Point out each Plasmodium parasite and each leukocyte.
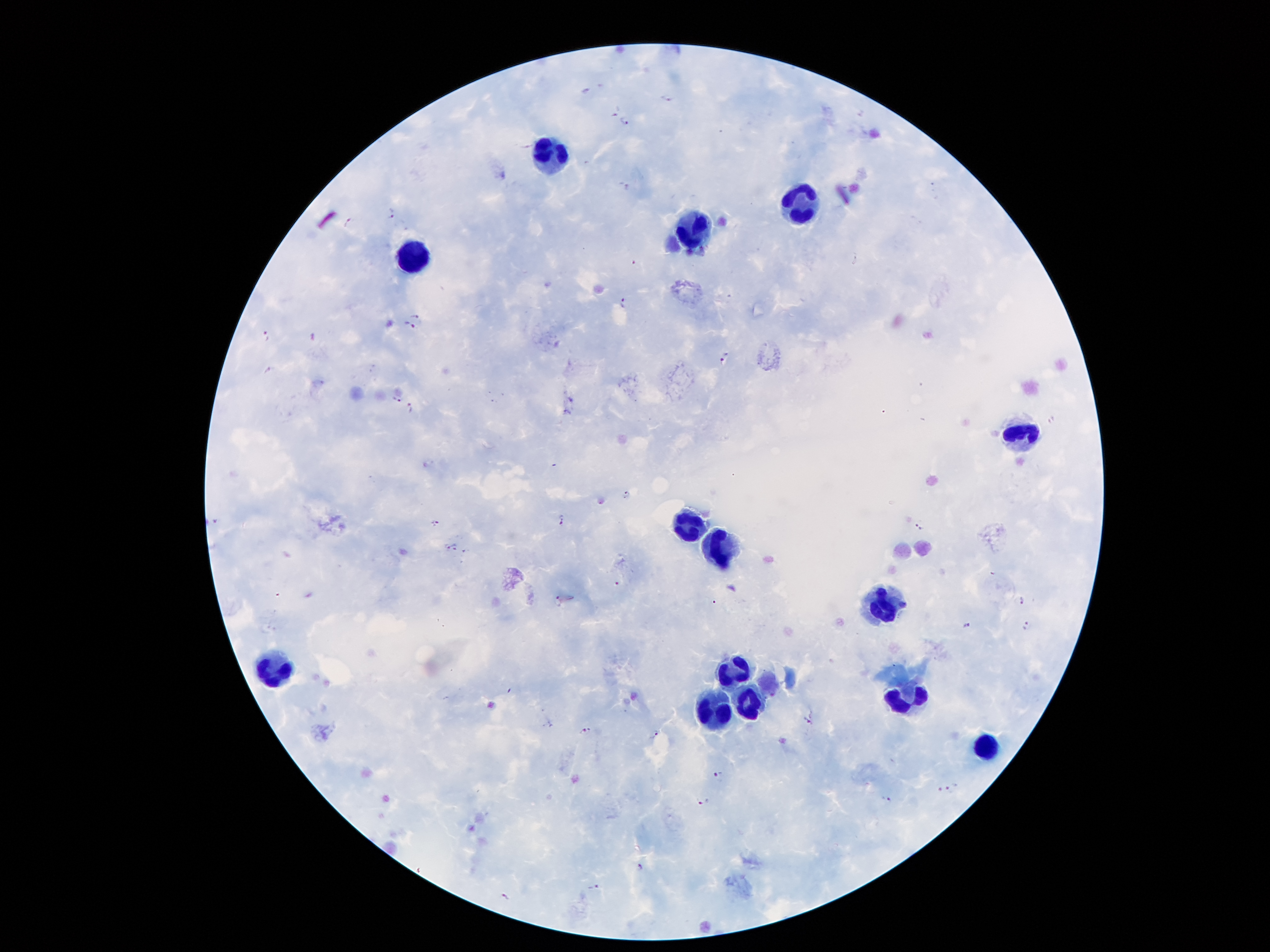

Approximate centers as [x, y] in pixels.
Plasmodium parasites: [587, 91], [669, 98], [624, 121], [627, 186], [391, 212], [347, 221], [622, 301], [419, 315], [409, 325], [266, 335], [724, 359], [270, 370], [394, 399], [410, 407], [627, 496], [560, 519], [434, 523], [918, 526], [446, 546], [455, 548], [618, 584], [559, 599], [1023, 601], [967, 625], [1026, 625], [810, 720], [585, 731], [656, 733], [719, 776], [951, 789], [940, 790], [888, 799], [704, 803], [639, 868], [594, 888], [505, 897].
Leukocytes: [546, 157], [801, 204], [693, 229], [410, 259], [1020, 433], [689, 522], [723, 548], [879, 607], [730, 668], [277, 676], [750, 700], [904, 704], [713, 708], [984, 748].

Thick blood film. Single field of view. Patient malaria status: infected with Plasmodium falciparum. Giemsa stain. Image is 1270×952 pixels. 100x magnification. Smartphone photograph taken through the microscope eyepiece.